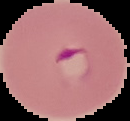
result: malaria parasites detected
image_type: segmented cell region on a black background
preparation: thin blood film
image_size: 130×121 pixels